Outline each Plasmodium falciparum-infected red blood cell.
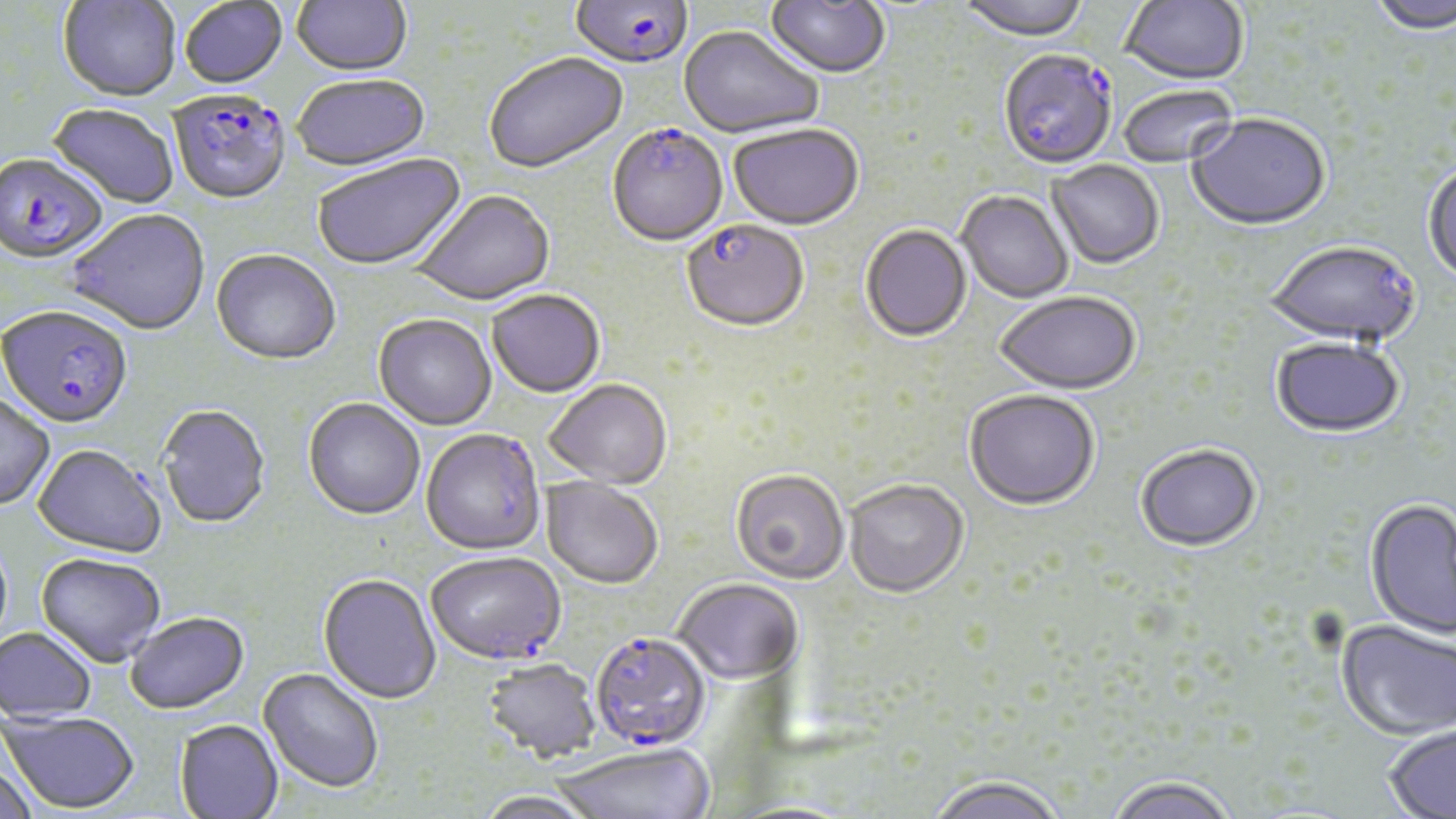

Approximate bounding boxes as (x1,y1)-(x2,y2) corner pairs in pixels.
Plasmodium falciparum-infected red blood cells: (569,0)-(693,73), (999,52)-(1117,171), (168,91)-(292,207), (607,127)-(728,250), (0,155)-(108,265), (682,221)-(809,335), (1,307)-(133,429), (426,553)-(567,667), (589,634)-(711,753).

{
  "slide_level_diagnosis": "Plasmodium falciparum",
  "preparation": "thin blood smear",
  "uninfected_red_blood_cell_locations": "approximate bounding boxes as (x1,y1)-(x2,y2) corner pairs in pixels: (290,0)-(413,79), (764,0)-(891,81), (956,0)-(1090,44), (1119,0)-(1248,87), (1365,0)-(1456,37), (57,1)-(181,104), (179,1)-(288,91), (678,26)-(823,141), (485,54)-(629,175), (292,77)-(431,175), (1119,86)-(1236,169), (46,104)-(180,211), (1186,115)-(1331,234), (728,126)-(865,234), (312,154)-(468,273), (1047,161)-(1165,271), (1423,163)-(1456,288), (411,192)-(556,308), (956,192)-(1073,304), (67,212)-(210,337), (860,226)-(972,344), (1263,244)-(1420,349), (211,251)-(341,368), (487,291)-(605,400), (995,294)-(1141,397), (372,316)-(497,432), (1270,340)-(1406,441), (544,381)-(672,491), (0,392)-(56,510), (964,392)-(1100,513), (302,399)-(425,522), (156,404)-(271,529), (420,430)-(547,558), (33,444)-(166,558), (1135,447)-(1262,554), (730,472)-(849,586), (540,477)-(663,591), (844,482)-(969,600), (1364,499)-(1456,641), (36,552)-(167,667), (318,574)-(441,705), (673,580)-(804,686), (125,611)-(249,714), (1335,621)-(1456,743), (0,626)-(97,723), (481,659)-(602,765), (258,668)-(384,793), (2,710)-(139,813), (174,719)-(283,818), (1382,724)-(1456,819), (554,745)-(714,819), (0,759)-(38,819), (927,778)-(1066,819), (1104,778)-(1238,819), (474,791)-(603,819)",
  "image_size": "1456×819 pixels",
  "field_of_view": "one of a larger specimen",
  "magnification": "1000x",
  "modality": "light microscopy",
  "stain": "May-Grünwald-Giemsa"
}